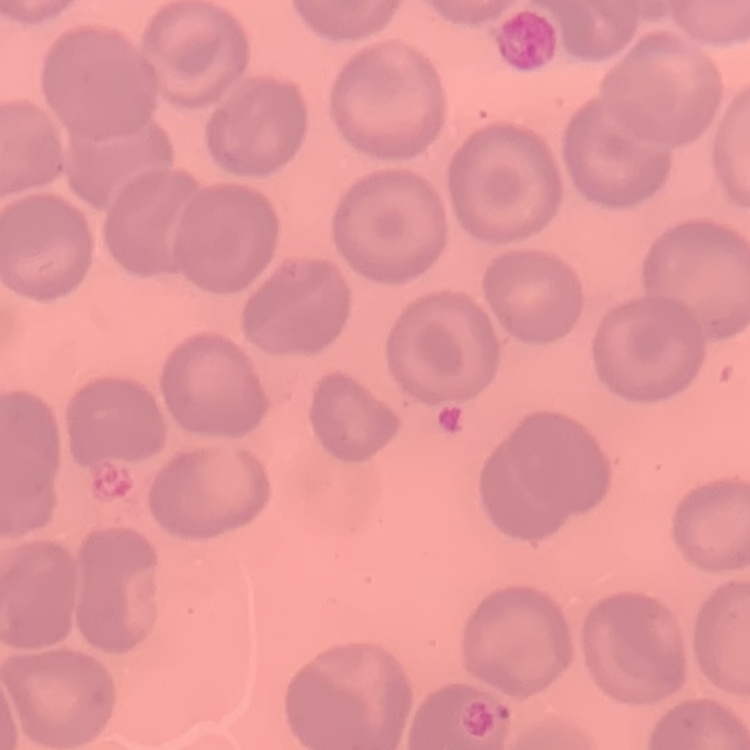
red_blood_cell_morphology: no rouleaux formation
stain: Field's or Giemsa
image_type: one tile cut from a larger photomicrograph
preparation: thin peripheral smear